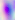
{
  "magnification": "400x",
  "modality": "micrograph",
  "identification": "Toxoplasma gondii"
}